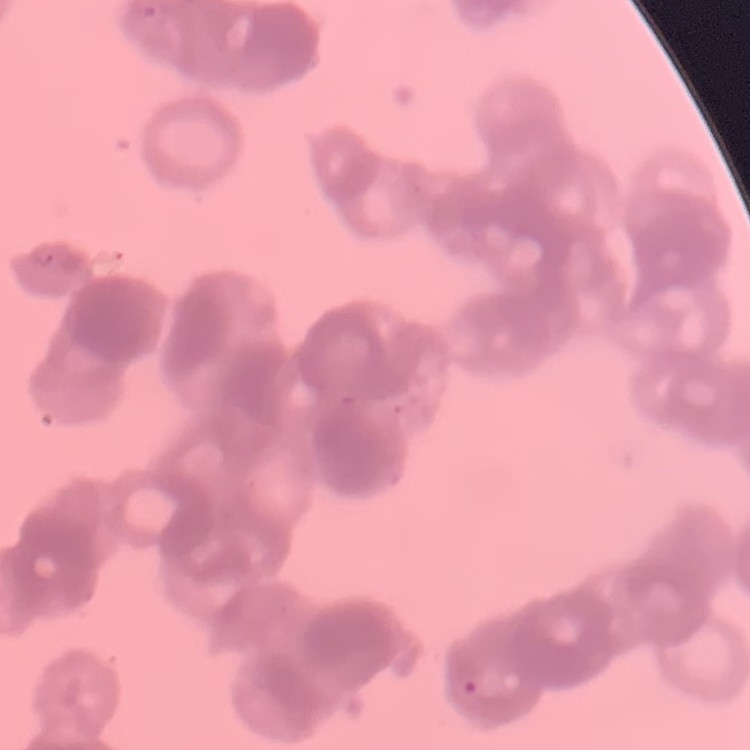
erythrocyte_morphology: rouleaux formation
stain: Field's or Giemsa
image_type: one tile cut from a larger photomicrograph
preparation: thin peripheral smear